Comment on the morphology of the erythrocytes.
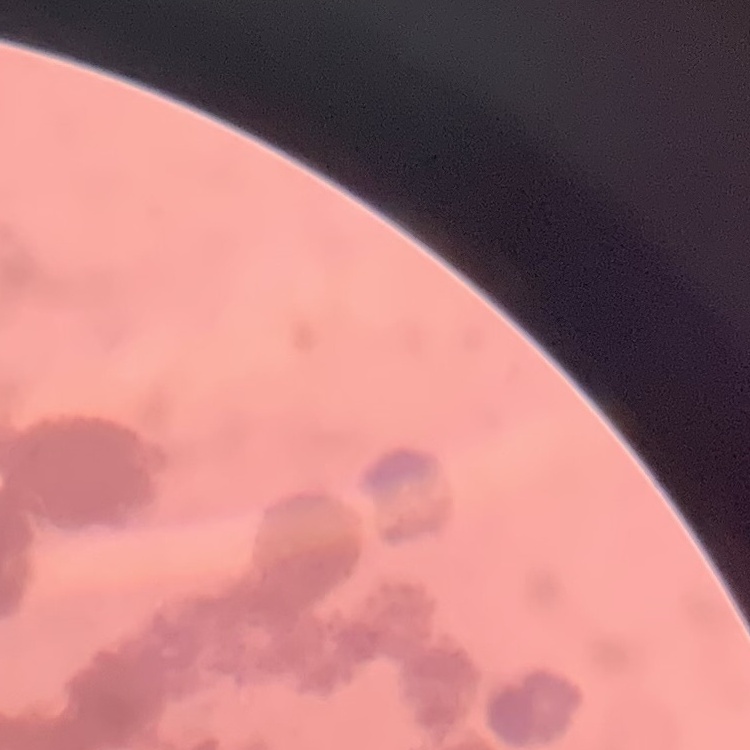
They show rouleaux formation.

Thin peripheral smear. One tile cut from a larger photomicrograph. Stained with either Field's or Giemsa.